Assess the morphology of the red blood cells.
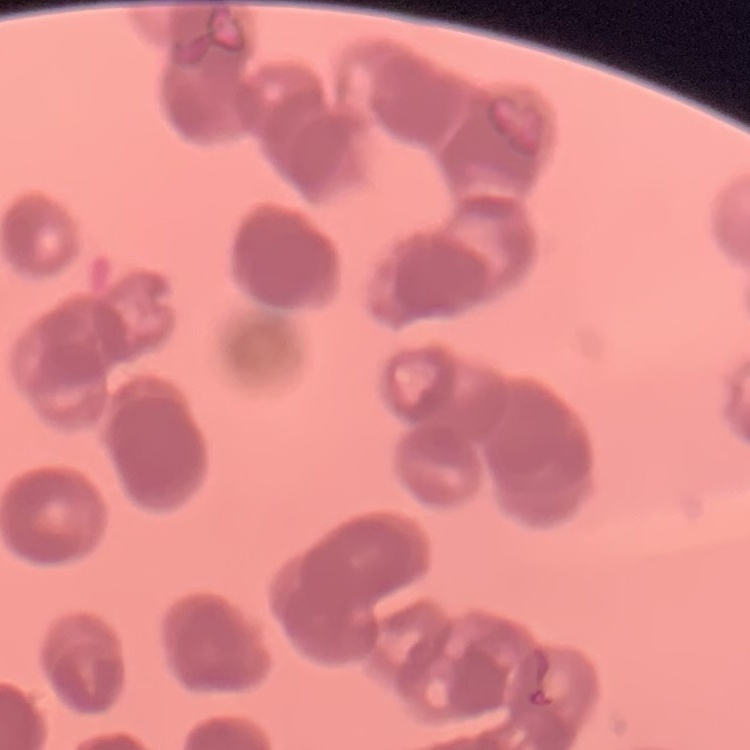

They show rouleaux formation.

One tile cut from a larger photomicrograph. Field's or Giemsa stain. Thin blood film.